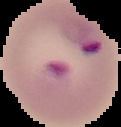
{
  "result": "Plasmodium parasites identified",
  "preparation": "thin blood smear",
  "image_size": "121×127 pixels",
  "image_type": "cell region segmented out of the field of view; surrounding area masked to black"
}